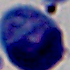
Summary:
  - Magnification: 1000x
  - Modality: photomicrograph
  - Identification: white blood cell